Report the malaria status of this cell.
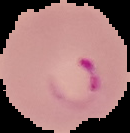
Parasitized.

Summary:
  - Image type: segmented cell region on a black background
  - Preparation: thin blood smear
  - Image size: 130×133 pixels